Classify this cell by malaria status.
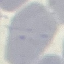
Uninfected.

stain: Giemsa
capture: smartphone through the microscope eyepiece
preparation: thin smear
image_type: automatically extracted cell patch, resized to 64 × 64 pixels